Describe the morphology of the red blood cells.
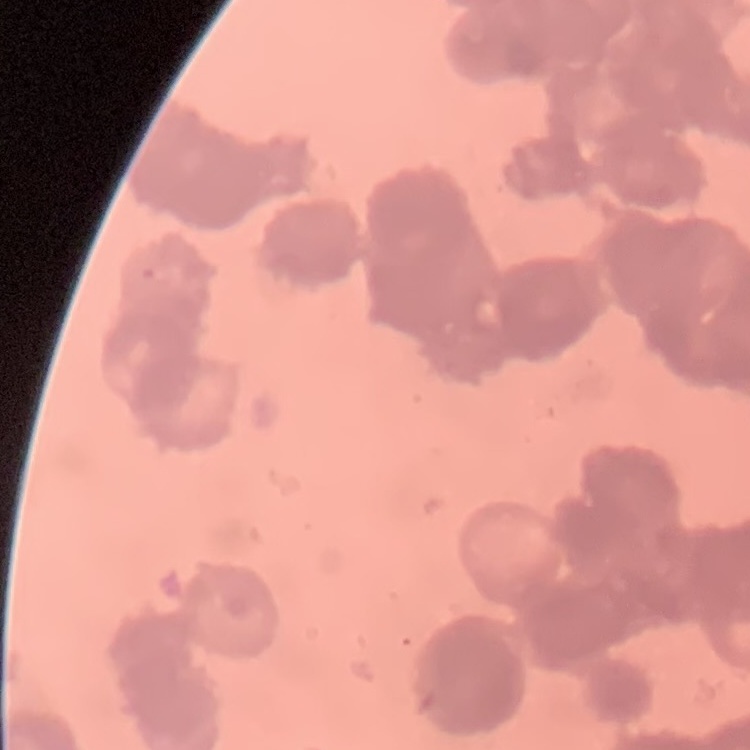

Rouleaux formation.

One tile cut from a larger photomicrograph. Field's or Giemsa stain. Thin blood smear.